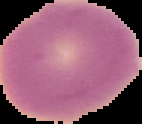
malaria status = uninfected
image type = cell region segmented out of the field of view; surrounding area masked to black
image size = 142×124 pixels
preparation = thin blood smear